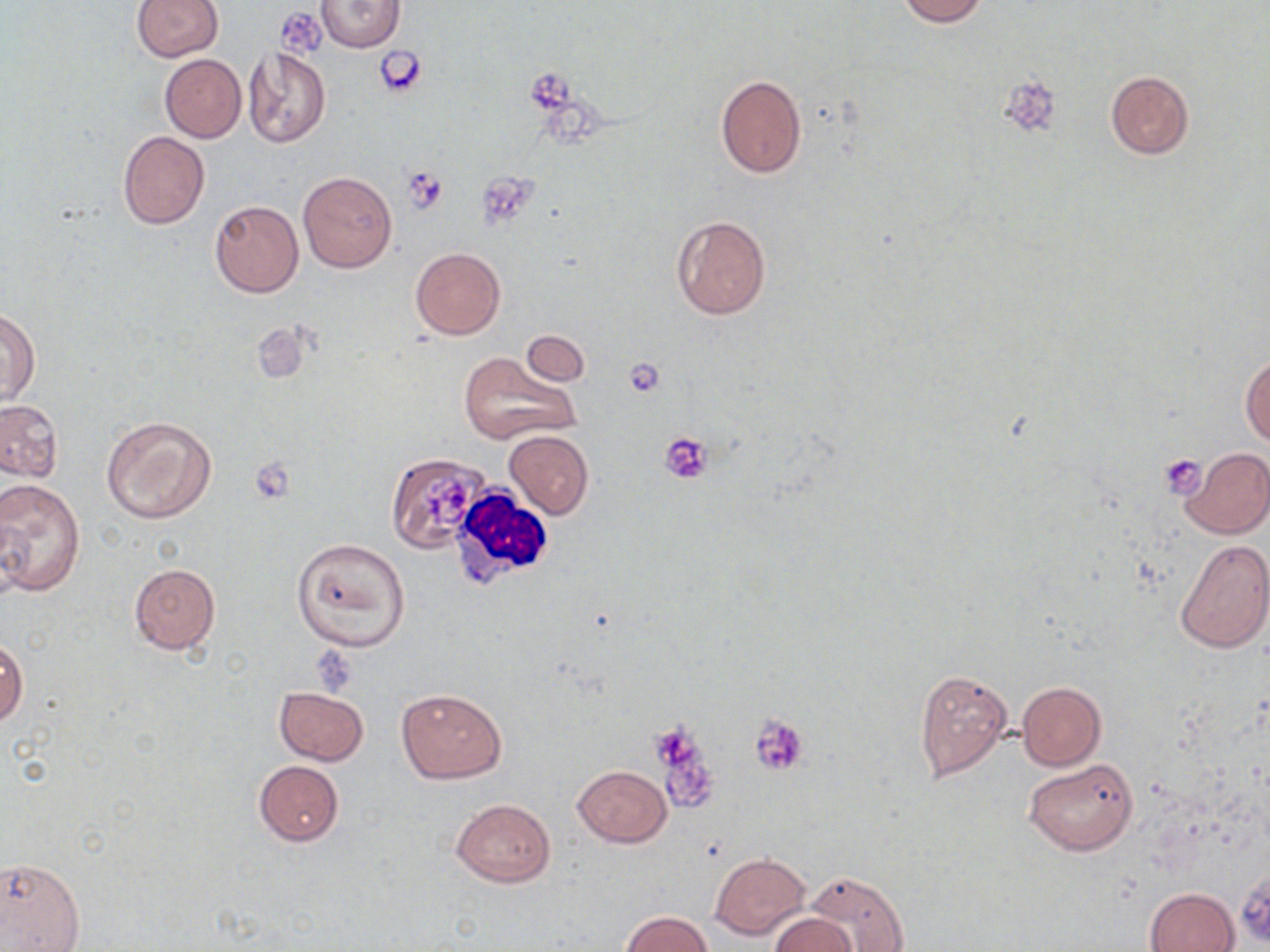

Summary:
  - Coordinate format: approximate bounding boxes as named x1/y1/x2/y2 corners in pixels
  - White blood cell locations: (x1=448, y1=484, x2=558, y2=588)
  - Platelet locations: (x1=279, y1=9, x2=321, y2=54), (x1=377, y1=47, x2=429, y2=97), (x1=525, y1=70, x2=577, y2=113), (x1=1004, y1=77, x2=1055, y2=132), (x1=403, y1=165, x2=448, y2=211), (x1=479, y1=172, x2=543, y2=224), (x1=624, y1=357, x2=665, y2=397), (x1=660, y1=431, x2=714, y2=483), (x1=1159, y1=454, x2=1207, y2=498), (x1=251, y1=459, x2=293, y2=497), (x1=421, y1=481, x2=470, y2=529), (x1=311, y1=648, x2=360, y2=695), (x1=747, y1=714, x2=809, y2=777), (x1=654, y1=727, x2=713, y2=812)
  - Uninfected red blood cell locations: (x1=131, y1=0, x2=224, y2=61), (x1=896, y1=0, x2=987, y2=25), (x1=314, y1=1, x2=405, y2=52), (x1=243, y1=47, x2=330, y2=148), (x1=160, y1=54, x2=246, y2=142), (x1=1105, y1=70, x2=1194, y2=159), (x1=715, y1=75, x2=807, y2=179), (x1=118, y1=130, x2=209, y2=229), (x1=297, y1=171, x2=397, y2=273), (x1=210, y1=201, x2=304, y2=297), (x1=671, y1=215, x2=772, y2=319), (x1=410, y1=247, x2=505, y2=340), (x1=1, y1=308, x2=39, y2=407), (x1=520, y1=331, x2=590, y2=386), (x1=496, y1=339, x2=598, y2=408), (x1=1241, y1=351, x2=1269, y2=449), (x1=459, y1=352, x2=580, y2=445), (x1=0, y1=400, x2=63, y2=481), (x1=101, y1=414, x2=217, y2=525), (x1=503, y1=429, x2=594, y2=518), (x1=1179, y1=447, x2=1270, y2=540), (x1=386, y1=452, x2=492, y2=553), (x1=0, y1=478, x2=86, y2=599), (x1=292, y1=537, x2=410, y2=651), (x1=1174, y1=540, x2=1270, y2=654), (x1=128, y1=563, x2=220, y2=655), (x1=0, y1=637, x2=28, y2=729), (x1=914, y1=669, x2=1013, y2=781), (x1=1016, y1=682, x2=1105, y2=770), (x1=275, y1=687, x2=368, y2=765), (x1=395, y1=687, x2=507, y2=783), (x1=1023, y1=759, x2=1138, y2=855), (x1=254, y1=761, x2=344, y2=847), (x1=572, y1=765, x2=672, y2=847), (x1=450, y1=798, x2=556, y2=887), (x1=709, y1=852, x2=811, y2=941), (x1=0, y1=854, x2=86, y2=952), (x1=804, y1=870, x2=908, y2=952), (x1=1146, y1=887, x2=1239, y2=952), (x1=623, y1=912, x2=711, y2=951), (x1=770, y1=913, x2=857, y2=952)
  - Slide-level diagnosis: negative for blood parasites
  - Image size: 1270×952 pixels
  - Magnification: 1000x
  - Modality: light microscopy
  - Preparation: thin blood film
  - Field of view: single
  - Stain: May-Grünwald-Giemsa